Classify this cell by malaria status.
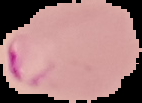
It is parasitized.

Summary:
  - Image type: cell region segmented out of the field of view; surrounding area masked to black
  - Preparation: thin blood film
  - Image size: 142×103 pixels